Identify the parasite.
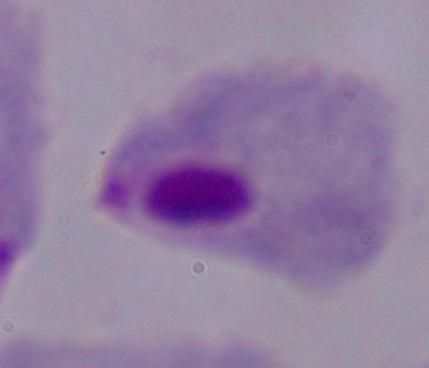

A trichomonad.

1000x magnification. Photomicrograph.